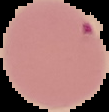
image_type: cell region segmented out of the field of view; surrounding area masked to black
preparation: thin blood smear
image_size: 109×112 pixels
malaria_status: parasitized